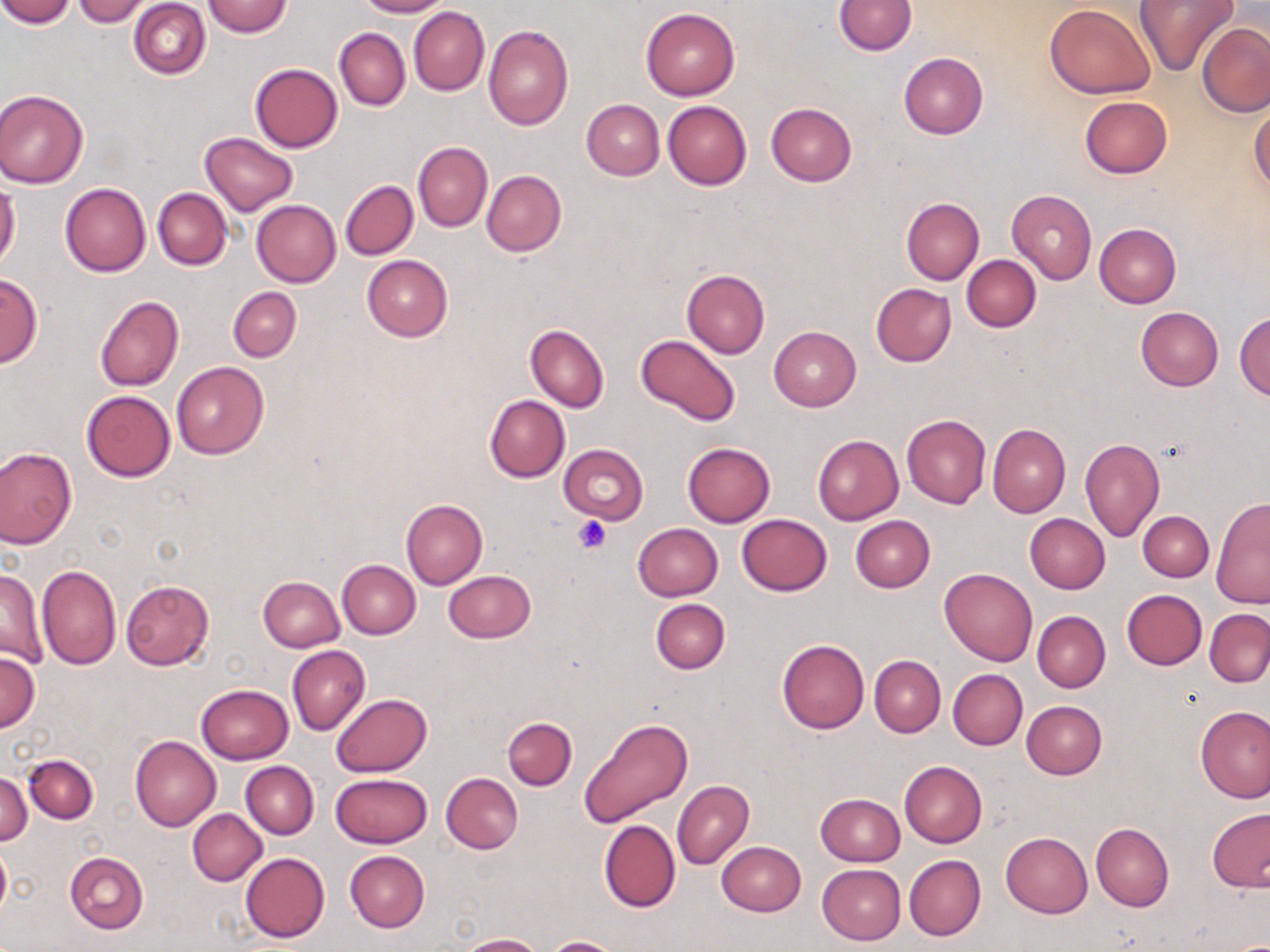

slide-level diagnosis = negative for blood parasites
platelet locations = approximate bounding boxes as (x1, y1, x2, y2) in pixels: (574, 517, 610, 553)
field of view = one of a larger specimen
uninfected red blood cell locations = approximate bounding boxes as (x1, y1, x2, y2) in pixels: (0, 0, 74, 27), (355, 0, 451, 17), (833, 0, 917, 55), (1133, 0, 1236, 77), (74, 1, 153, 25), (128, 1, 210, 79), (203, 1, 293, 37), (1043, 3, 1155, 99), (409, 7, 489, 95), (640, 7, 740, 100), (483, 23, 573, 131), (1198, 23, 1269, 116), (335, 27, 410, 111), (899, 51, 988, 138), (250, 64, 343, 152), (0, 88, 89, 188), (1079, 97, 1171, 178), (581, 99, 665, 180), (663, 100, 751, 189), (766, 102, 857, 185), (1249, 107, 1270, 194), (201, 132, 297, 215), (413, 142, 492, 231), (481, 171, 567, 257), (340, 180, 418, 260), (59, 181, 151, 277), (0, 184, 20, 269), (153, 187, 231, 270), (1006, 189, 1097, 285), (900, 197, 984, 285), (252, 200, 341, 286), (1094, 223, 1182, 307), (361, 255, 454, 341), (962, 255, 1040, 332), (681, 270, 770, 357), (0, 274, 42, 367), (871, 283, 957, 367), (228, 287, 301, 362), (94, 296, 184, 392), (1135, 306, 1223, 391), (1234, 311, 1269, 398), (525, 324, 609, 413), (768, 326, 861, 411), (636, 335, 740, 425), (170, 361, 269, 459), (82, 390, 176, 481), (485, 395, 570, 482), (901, 414, 991, 509), (987, 425, 1070, 517), (813, 434, 903, 525), (1079, 438, 1164, 541), (682, 443, 775, 527), (558, 444, 648, 524), (0, 447, 77, 549), (1212, 496, 1270, 607), (400, 498, 488, 589), (1139, 510, 1214, 582), (736, 513, 832, 595), (1025, 513, 1110, 593), (850, 515, 935, 593), (632, 523, 723, 601), (337, 560, 420, 639), (36, 564, 122, 670), (1, 567, 48, 669), (939, 568, 1037, 666), (443, 571, 535, 643), (258, 576, 345, 652), (121, 578, 214, 670), (1121, 589, 1207, 670), (650, 599, 730, 675), (1204, 608, 1270, 688), (1032, 611, 1111, 693), (776, 639, 869, 734), (288, 645, 370, 734), (0, 651, 39, 730), (870, 655, 946, 737), (948, 670, 1027, 749), (196, 684, 293, 764), (331, 693, 431, 777), (1021, 701, 1107, 780), (1195, 706, 1270, 803), (578, 716, 694, 828), (502, 717, 577, 790), (131, 735, 221, 831), (23, 754, 98, 822), (898, 760, 987, 848), (241, 761, 319, 838), (0, 772, 31, 846), (331, 773, 431, 849), (442, 773, 523, 853), (673, 781, 754, 870), (816, 793, 904, 866), (1207, 806, 1270, 893), (187, 809, 267, 885), (599, 820, 680, 912), (1090, 823, 1174, 912), (1001, 832, 1092, 917), (0, 839, 11, 924), (717, 842, 805, 916), (64, 851, 148, 934), (344, 851, 429, 933), (241, 852, 330, 943), (904, 854, 986, 940), (817, 863, 906, 944), (457, 932, 544, 951), (544, 936, 624, 952)
image size = 1270×952 pixels
stain = May-Grünwald-Giemsa
magnification = 1000x
preparation = thin blood film
modality = optical microscopy